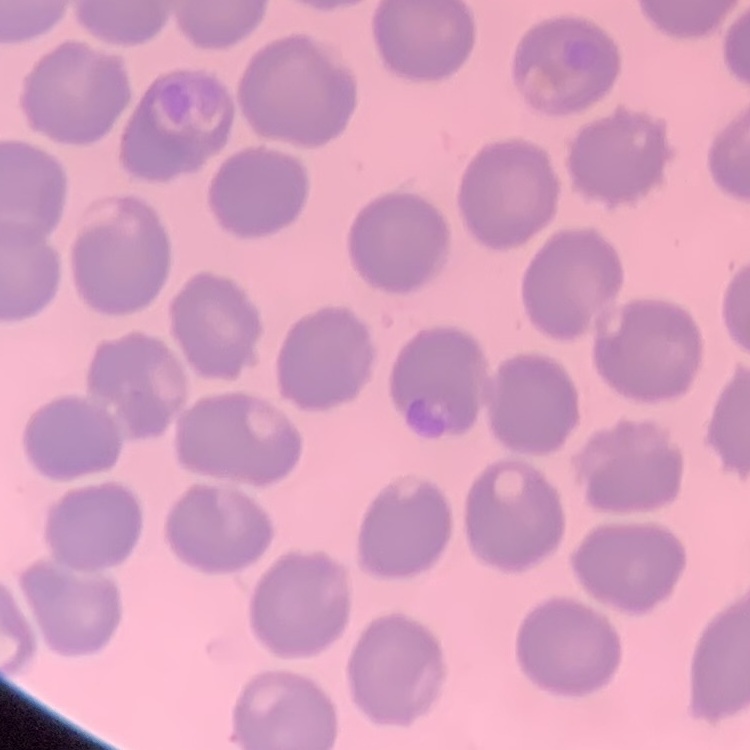
erythrocyte morphology = no rouleaux formation
image type = one tile cut from a larger photomicrograph
preparation = thin blood film
stain = Field's or Giemsa